Identify the parasite.
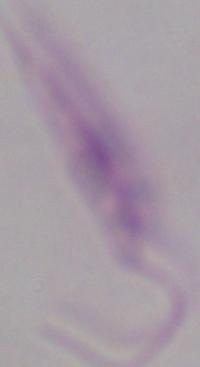

Leishmania.

Summary:
  - Magnification: 1000x
  - Modality: micrograph